Classify this cell by malaria status.
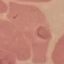
Parasitized.

Summary:
  - Preparation: thin smear
  - Stain: Giemsa
  - Image type: automatically extracted cell patch, resized to 64 × 64 pixels
  - Capture: smartphone camera at the microscope eyepiece